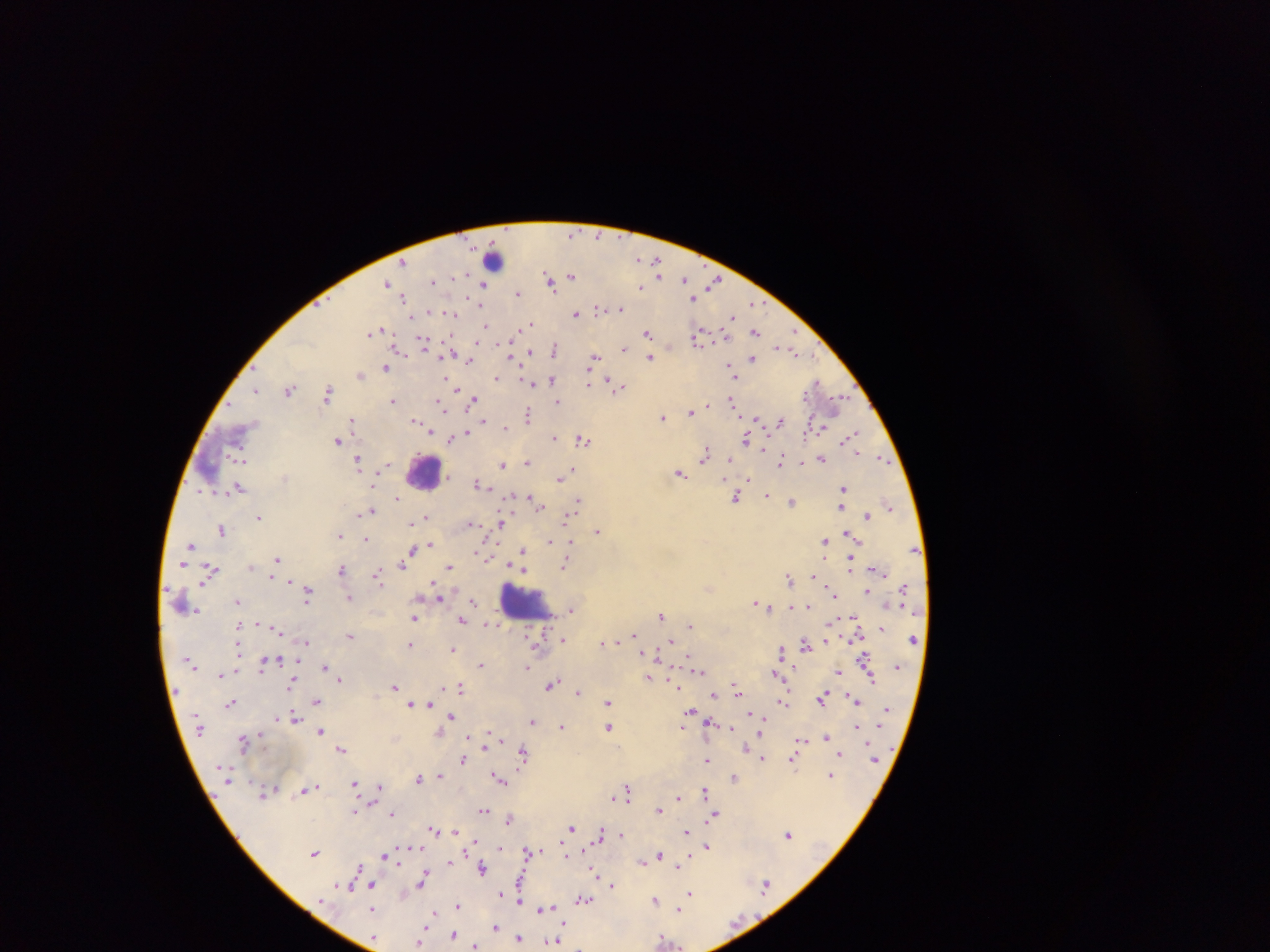
Approximate centers as {x, y} in pixels.
Summary:
  - Leukocyte locations: {425, 472}, {524, 602}
  - Plasmodium parasite locations (subset; some below the resolvable size): {572, 234}, {493, 259}, {639, 259}, {655, 260}, {403, 262}, {657, 267}, {659, 274}, {571, 275}, {434, 280}, {684, 280}, {550, 282}, {388, 283}, {714, 283}, {483, 285}, {640, 287}, {518, 293}, {404, 298}, {694, 299}, {753, 303}, {481, 305}, {598, 309}, {620, 309}, {576, 313}, {452, 314}, {731, 317}, {530, 323}, {486, 326}, {379, 331}, {755, 332}, {373, 333}, {648, 333}, {699, 336}, {423, 343}, {778, 347}, {451, 348}, {625, 349}, {554, 350}, {530, 351}, {792, 351}, {650, 357}, {594, 358}, {753, 358}, {469, 361}, {386, 368}, {731, 371}, {360, 375}, {497, 377}, {525, 380}, {552, 380}, {447, 381}, {610, 381}, {531, 383}, {816, 383}, {589, 384}, {618, 388}, {256, 390}, {290, 390}, {328, 393}, {392, 400}, {474, 400}, {732, 400}, {840, 401}, {557, 402}, {441, 404}, {691, 411}, {528, 414}, {663, 418}, {756, 420}, {352, 421}, {415, 421}, {780, 421}, {483, 422}, {506, 427}, {430, 432}, {465, 432}, {850, 436}, {554, 438}, {746, 439}, {451, 440}, {583, 440}, {338, 441}, {706, 455}, {821, 458}, {882, 459}, {358, 460}, {782, 460}, {242, 461}, {728, 461}, {527, 463}, {502, 464}, {386, 466}, {571, 470}, {679, 473}, {560, 478}, {749, 479}, {477, 484}, {239, 488}, {843, 488}, {768, 494}, {736, 497}, {397, 498}, {530, 498}, {578, 500}, {841, 502}, {793, 503}, {536, 504}, {889, 505}, {370, 510}, {867, 516}, {427, 517}, {259, 518}, {567, 518}, {470, 524}, {500, 524}, {221, 529}, {597, 530}, {849, 534}, {339, 536}, {366, 539}, {825, 541}, {549, 542}, {190, 544}, {571, 544}, {430, 545}, {522, 550}, {409, 556}, {278, 559}, {403, 564}, {566, 564}, {851, 564}, {449, 566}, {210, 570}, {341, 570}, {274, 575}, {377, 575}, {815, 576}, {789, 578}, {867, 592}, {308, 594}, {833, 595}, {439, 597}, {349, 599}, {237, 601}, {473, 601}, {756, 602}, {765, 606}, {809, 606}, {571, 610}, {661, 615}, {414, 618}, {462, 620}, {690, 626}, {882, 628}, {278, 630}, {350, 635}, {633, 635}, {563, 639}, {678, 639}, {913, 639}, {826, 640}, {306, 642}, {672, 642}, {602, 643}, {806, 643}, {411, 645}, {452, 649}, {781, 651}, {865, 657}, {264, 665}, {482, 665}, {325, 667}, {527, 667}, {699, 671}, {839, 672}, {221, 675}, {776, 675}, {649, 678}, {870, 678}, {340, 680}, {292, 683}, {551, 684}, {395, 687}, {461, 688}, {738, 689}, {578, 691}, {714, 695}, {851, 697}, {822, 699}, {317, 701}, {857, 701}, {609, 702}, {783, 702}, {428, 703}, {230, 704}, {412, 704}, {690, 710}, {293, 716}, {451, 716}, {532, 721}, {713, 722}, {683, 726}, {856, 726}, {562, 727}, {609, 727}, {320, 731}, {761, 733}, {825, 736}, {244, 741}, {801, 741}, {486, 743}, {746, 749}, {342, 750}, {523, 752}, {841, 753}, {762, 758}, {463, 759}, {793, 759}, {707, 760}, {875, 761}, {830, 775}, {440, 776}, {419, 777}, {734, 777}, {500, 778}, {355, 784}, {380, 787}, {308, 788}, {628, 790}, {705, 791}, {614, 797}, {678, 797}, {659, 809}, {484, 811}, {393, 814}, {715, 815}, {509, 819}, {572, 828}, {434, 829}, {685, 832}, {601, 834}, {620, 834}, {788, 834}, {707, 846}, {530, 851}, {315, 852}, {566, 855}, {659, 855}, {387, 856}, {643, 860}, {450, 862}, {678, 865}, {482, 868}, {526, 871}, {422, 880}, {371, 885}, {612, 885}, {765, 885}, {349, 888}, {690, 894}, {519, 898}, {583, 900}, {655, 900}, {372, 908}, {458, 908}, {544, 909}, {679, 909}, {432, 914}, {494, 928}, {454, 934}, {560, 935}, {519, 939}, {664, 939}, {419, 940}, {554, 941}, {475, 946}
  - Field of view: single
  - Country: Ghana
  - Capture: mobile-phone photograph through a microscope
  - Preparation: thick blood film
  - Image size: 1270×952 pixels